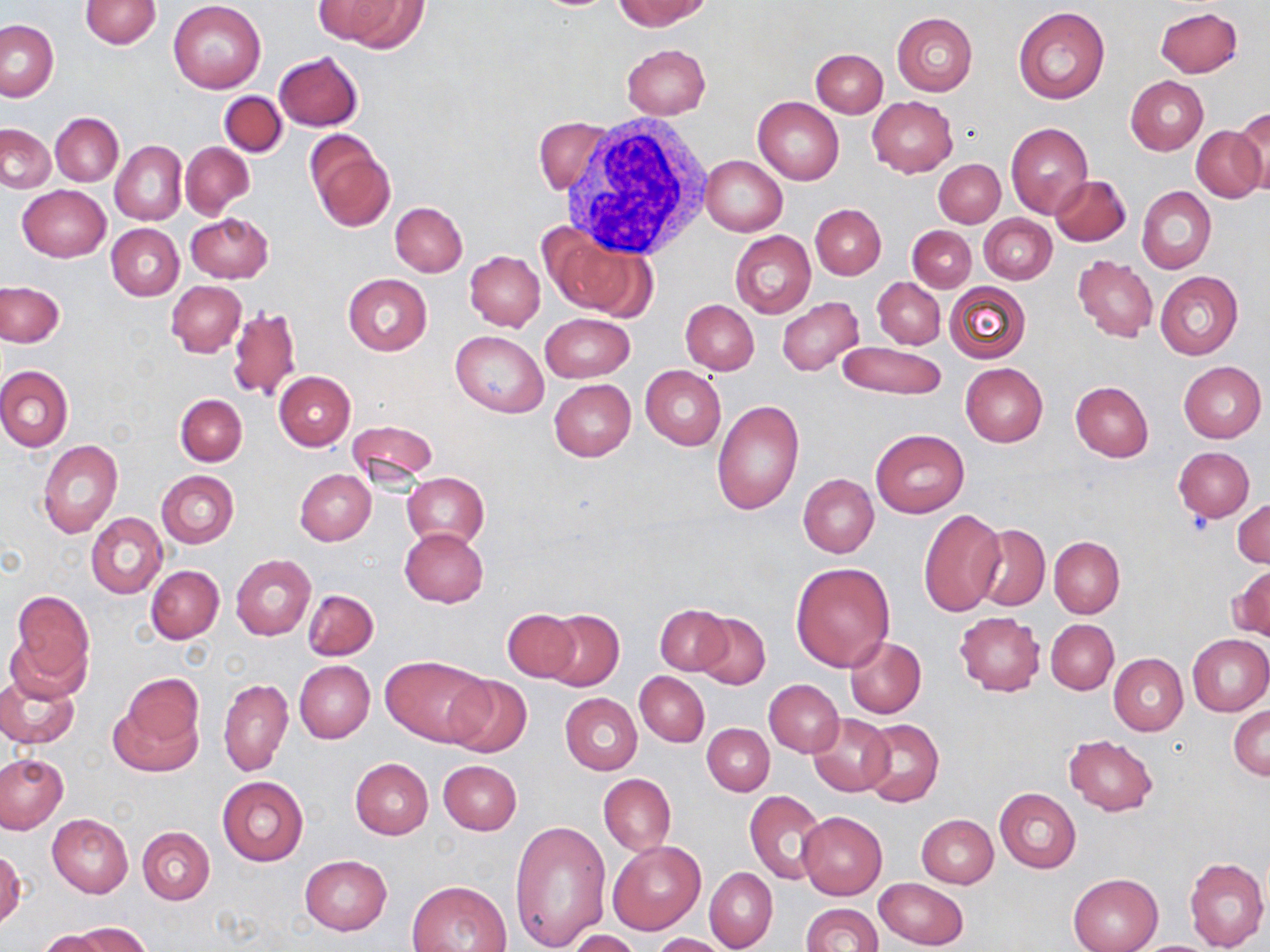

{
  "slide_level_diagnosis": "negative for blood parasites",
  "platelet_locations": "approximate bounding boxes as (x1,y1)-(x2,y2) corner pairs in pixels: (1182,514)-(1212,537)",
  "image_size": "1270×952 pixels",
  "field_of_view": "single",
  "modality": "light microscopy",
  "preparation": "thin blood film",
  "stain": "May-Grünwald-Giemsa",
  "white_blood_cell_locations": "approximate bounding boxes as (x1,y1)-(x2,y2) corner pairs in pixels: (552,115)-(717,257)",
  "magnification": "1000x",
  "uninfected_red_blood_cell_locations": "approximate bounding boxes as (x1,y1)-(x2,y2) corner pairs in pixels: (613,0)-(707,30), (80,1)-(161,48), (168,1)-(266,94), (328,1)-(431,51), (1155,6)-(1243,78), (1012,7)-(1110,104), (892,13)-(977,96), (1,20)-(58,100), (621,43)-(710,120), (811,48)-(887,117), (273,52)-(363,131), (1125,76)-(1208,155), (218,91)-(287,157), (753,95)-(844,184), (867,96)-(958,177), (1231,111)-(1270,196), (51,112)-(122,186), (534,119)-(610,194), (1006,122)-(1094,219), (1,123)-(55,193), (1191,125)-(1266,202), (305,133)-(395,232), (111,140)-(187,226), (180,142)-(254,216), (699,155)-(787,236), (934,159)-(1004,227), (1050,175)-(1130,246), (18,185)-(109,261), (1137,186)-(1216,273), (390,201)-(467,277), (811,204)-(886,280), (186,213)-(272,283), (980,214)-(1056,284), (107,224)-(184,301), (907,226)-(976,292), (545,229)-(651,320), (730,231)-(815,318), (464,250)-(544,331), (1073,255)-(1157,341), (1155,271)-(1243,360), (343,274)-(431,355), (872,277)-(945,349), (167,280)-(246,356), (0,281)-(65,346), (944,282)-(1030,364), (777,297)-(863,376), (680,300)-(759,374), (227,305)-(302,402), (541,312)-(634,383), (451,330)-(548,418), (838,342)-(945,399), (1177,361)-(1266,443), (960,363)-(1048,447), (0,366)-(73,451), (641,366)-(727,450), (274,370)-(355,450), (548,378)-(636,461), (1071,382)-(1153,462), (176,395)-(246,466), (711,399)-(803,512), (347,418)-(437,485), (870,429)-(969,518), (38,440)-(123,537), (1173,446)-(1254,521), (296,468)-(376,545), (156,470)-(239,548), (402,471)-(489,550), (798,474)-(878,558), (1233,499)-(1270,568), (918,507)-(1006,617), (86,513)-(167,598), (972,525)-(1050,611), (399,528)-(488,607), (1050,536)-(1124,619), (232,554)-(316,640), (791,562)-(895,671), (147,565)-(224,643), (1232,565)-(1270,642), (303,589)-(378,660), (10,590)-(94,691), (656,605)-(730,675), (502,608)-(580,681), (543,609)-(625,692), (695,612)-(770,690), (953,612)-(1046,696), (1046,619)-(1119,694), (1186,633)-(1270,716), (845,636)-(926,718), (1108,653)-(1188,735), (380,654)-(491,746), (294,660)-(375,743), (0,668)-(81,750), (635,672)-(709,746), (443,674)-(532,758), (219,678)-(292,775), (764,679)-(844,757), (108,691)-(203,777), (559,693)-(641,775), (1229,704)-(1270,779), (808,713)-(894,796), (859,719)-(944,807), (703,723)-(774,795), (1064,734)-(1158,815), (0,754)-(67,831), (350,757)-(434,838), (438,760)-(521,835), (599,774)-(676,855), (217,775)-(309,866), (994,788)-(1081,872), (745,790)-(828,884), (798,812)-(887,899), (47,814)-(133,897), (916,814)-(998,888), (510,818)-(610,951), (137,826)-(215,905), (609,840)-(705,934), (1,847)-(24,929), (299,854)-(392,935), (1184,856)-(1268,952), (704,867)-(778,951), (1068,874)-(1162,952), (874,878)-(969,950), (407,881)-(511,952), (800,903)-(883,952), (72,923)-(150,952), (568,930)-(642,952), (37,931)-(111,952), (653,932)-(732,952)"
}